Report the malaria status of this cell.
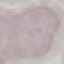

Uninfected.

Cell patch, automatically extracted from a larger field of view and resized to 64 × 64 pixels. Giemsa stain. Acquired by smartphone through the microscope eyepiece. Thin smear of blood.